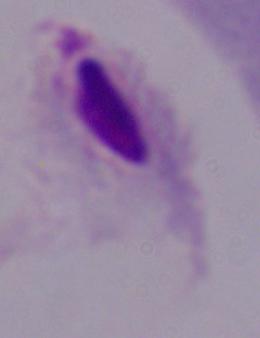

Summary:
  - Identification: trichomonad
  - Magnification: 1000x
  - Modality: photomicrograph